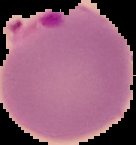 Image is 136×145 pixels. From a thin blood smear. Malaria status: parasitized. Segmented cell region on a black background.